Identify the parasite.
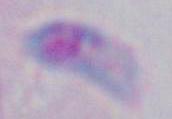
Toxoplasma gondii.

Summary:
  - Modality: micrograph
  - Magnification: 1000x